Classify this cell by malaria status.
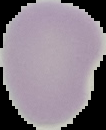

It is uninfected.

Image is 106×130 pixels. The area outside the segmented cell region is set to black. From a thin blood smear.